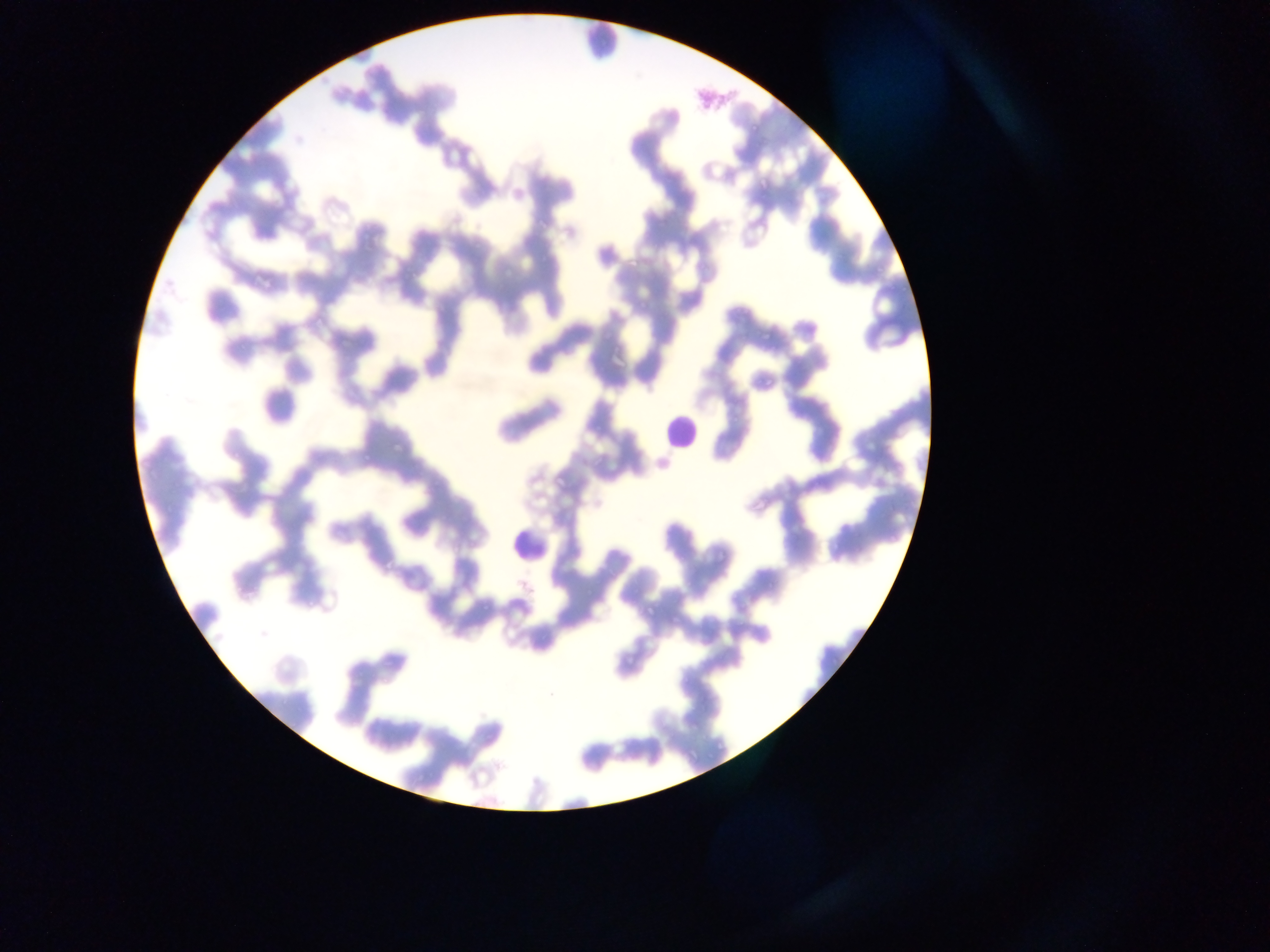

Approximate bounding boxes as (left, top, right, bottom) in pixels.
Summary:
  - Malaria parasite locations: (623, 258, 636, 268), (638, 301, 652, 313), (757, 329, 770, 343), (762, 372, 773, 394), (392, 441, 406, 455), (358, 445, 374, 464), (557, 472, 572, 493), (713, 543, 730, 561), (381, 558, 395, 569), (639, 601, 662, 618), (670, 610, 685, 626), (623, 648, 637, 672), (382, 649, 400, 673)
  - Leukocyte locations: (575, 17, 627, 63), (658, 406, 699, 455), (509, 519, 554, 569)
  - Field of view: single
  - Image size: 1270×952 pixels
  - Preparation: thin blood film
  - Capture: mobile-phone photograph through a microscope
  - Country: Ghana